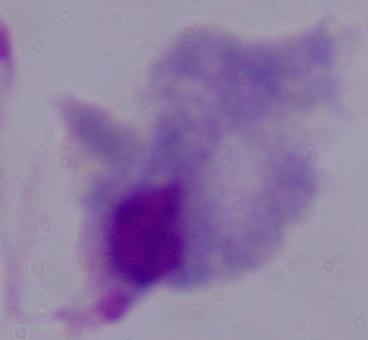

Photomicrograph. A trichomonad is seen. 1000x magnification.